Identify the cell.
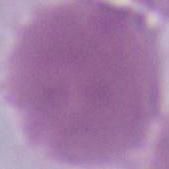
This is an erythrocyte.

Summary:
  - Magnification: 1000x
  - Modality: micrograph